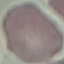
Summary:
  - Result: no malaria parasites seen
  - Stain: Giemsa
  - Image type: cell patch, automatically extracted from a larger field of view and resized to 64 × 64 pixels
  - Capture: smartphone camera at the microscope eyepiece
  - Preparation: thin blood film